Assess this cell for malaria.
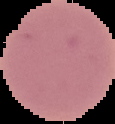

It is uninfected.

preparation = thin blood smear
image type = cell region segmented out of the field of view; surrounding area masked to black
image size = 115×124 pixels